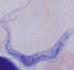 A trypanosome is seen. 1000x magnification. Micrograph.